Locate cells.
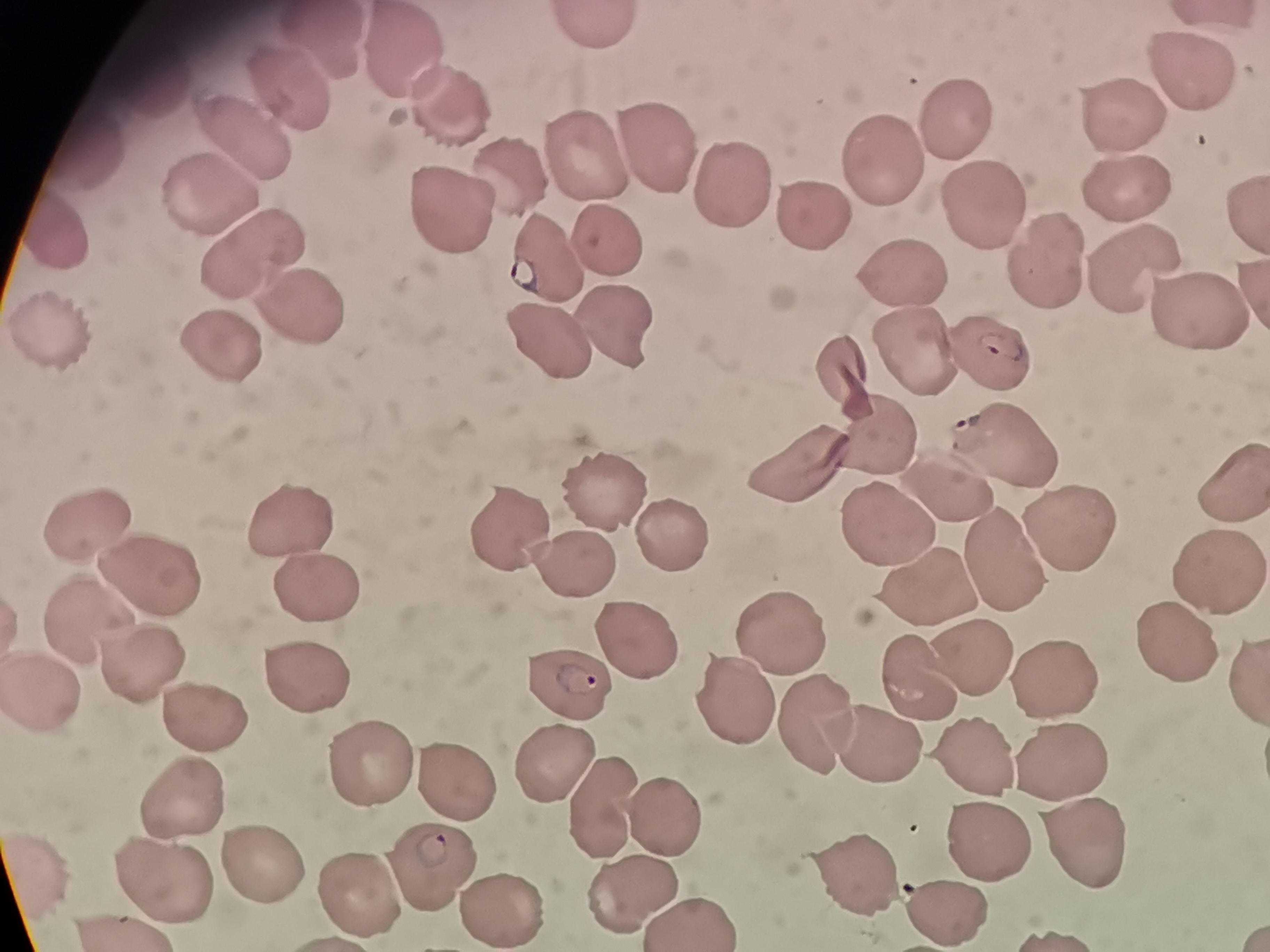
Approximate object centers, in pixels from the top-left corner.
Cells: (x=593, y=27), (x=327, y=50), (x=406, y=61), (x=1182, y=65), (x=154, y=78), (x=296, y=94), (x=442, y=115), (x=1119, y=117), (x=954, y=126), (x=258, y=133), (x=653, y=145), (x=96, y=153), (x=868, y=167), (x=587, y=170), (x=216, y=175), (x=510, y=180), (x=738, y=186), (x=1131, y=196), (x=437, y=208), (x=983, y=208), (x=805, y=214), (x=62, y=235), (x=242, y=247), (x=612, y=248), (x=1047, y=261), (x=1124, y=264), (x=551, y=271), (x=909, y=285), (x=1183, y=304), (x=311, y=311), (x=66, y=334), (x=544, y=339), (x=614, y=339), (x=223, y=342), (x=912, y=350), (x=990, y=358), (x=852, y=375), (x=882, y=417), (x=1011, y=450), (x=802, y=471), (x=942, y=486), (x=604, y=493), (x=294, y=502), (x=95, y=518), (x=513, y=522), (x=1074, y=526), (x=668, y=531), (x=884, y=533), (x=1001, y=551), (x=572, y=558), (x=1219, y=564), (x=148, y=577), (x=931, y=586), (x=313, y=589), (x=86, y=612), (x=642, y=635), (x=1173, y=635), (x=782, y=640), (x=971, y=654), (x=143, y=665), (x=922, y=672), (x=1246, y=675), (x=308, y=678), (x=572, y=681), (x=1059, y=681), (x=58, y=688), (x=743, y=698), (x=208, y=717), (x=812, y=724), (x=875, y=741), (x=552, y=742), (x=359, y=748), (x=976, y=751), (x=1066, y=755), (x=452, y=775), (x=597, y=796), (x=182, y=800), (x=670, y=822), (x=977, y=827), (x=1088, y=837), (x=440, y=853), (x=266, y=861), (x=162, y=871), (x=858, y=873), (x=630, y=879), (x=360, y=889), (x=946, y=903).

{
  "image_size": "1270×952 pixels",
  "preparation": "thin smear",
  "field_of_view": "single",
  "capture": "smartphone through the microscope eyepiece",
  "stain": "Giemsa"
}